Assess this cell for malaria.
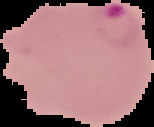
It is parasitized.

Summary:
  - Image type: segmented cell region on a black background
  - Image size: 154×127 pixels
  - Preparation: thin blood film